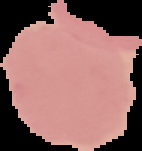
Summary:
  - Malaria status: uninfected
  - Preparation: thin blood film
  - Image size: 142×151 pixels
  - Image type: cell region segmented out of the field of view; surrounding area masked to black